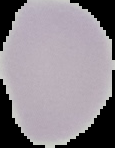 From a thin blood smear. The area outside the segmented cell region is set to black. Malaria status: uninfected. Image is 115×148 pixels.